Point out malaria parasites and leukocytes.
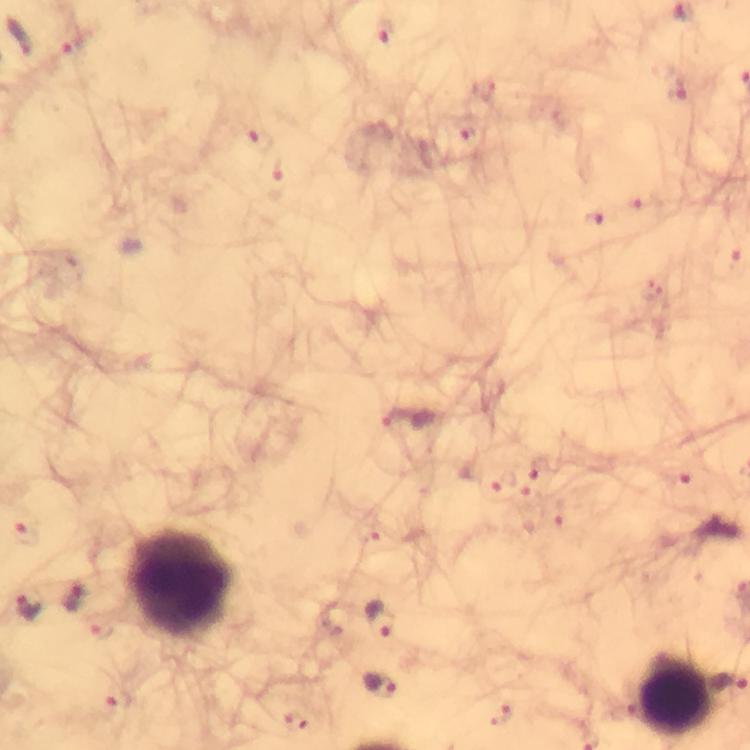
Approximate centers as [x, y] in pixels.
Malaria parasites: [73, 598], [28, 607], [381, 617], [381, 684].
Leukocytes: [181, 582], [677, 692].

Summary:
  - Preparation: thick blood smear
  - Magnification: 100x
  - Stain: Giemsa
  - Context: from a diagnostic examination for malaria
  - Image size: 750×750 pixels
  - Capture: smartphone photograph through a microscope
  - Immersion oil: applied
  - Cropped from: a single field of view